State which parasite is depicted.
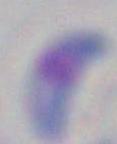

This is Toxoplasma gondii.

Captured at 1000x magnification. Micrograph.